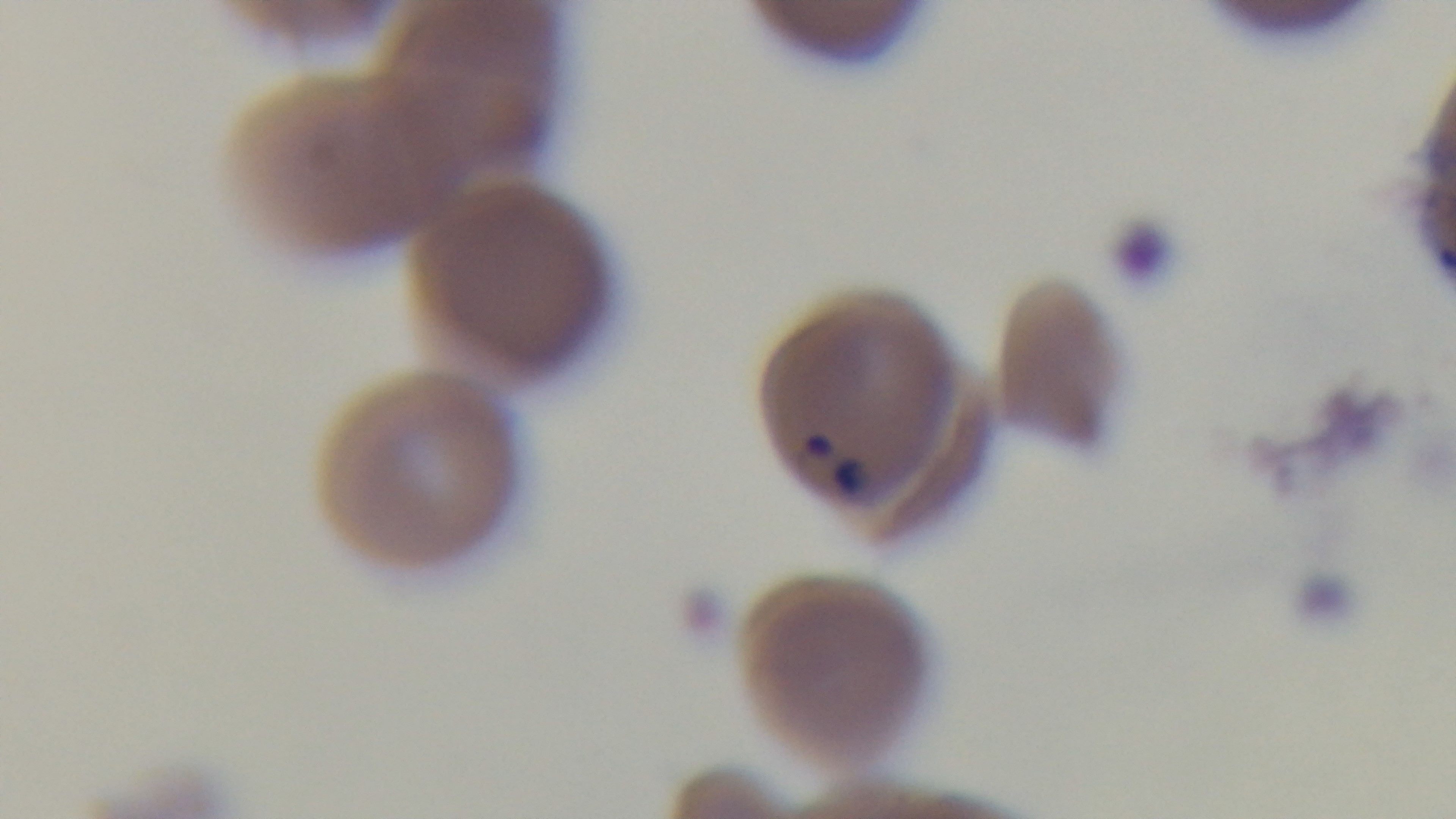

Summary:
  - Stain: Giemsa
  - Preparation: thin smear
  - Modality: light microscopy
  - Capture: mounted 4K digital camera
  - Objective: 100x oil immersion
  - Malaria status: positive
  - Field of view: one from the slide